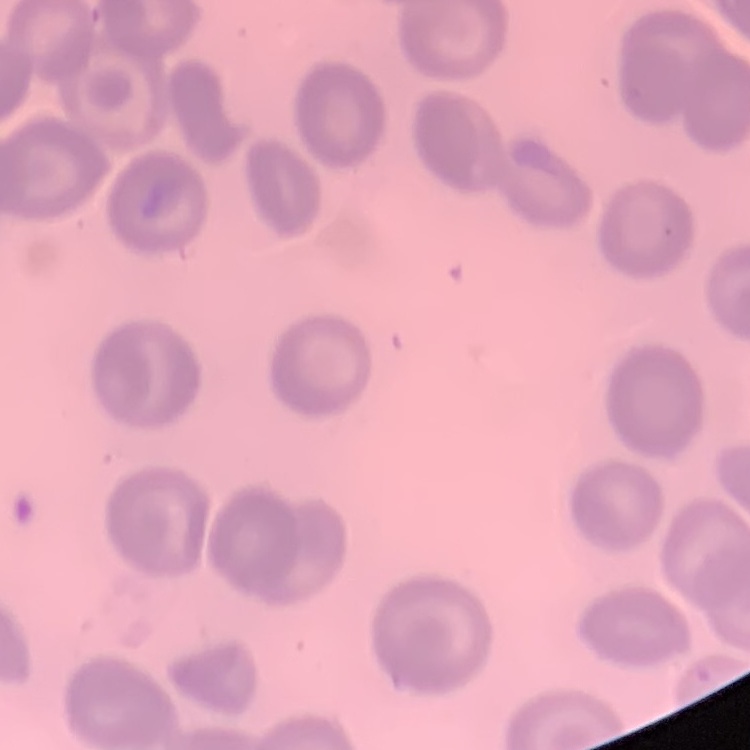
Summary:
  - Red blood cell morphology: no rouleaux formation
  - Preparation: thin peripheral smear
  - Stain: Field's or Giemsa
  - Image type: one tile cut from a larger photomicrograph